Identify the preparation type.
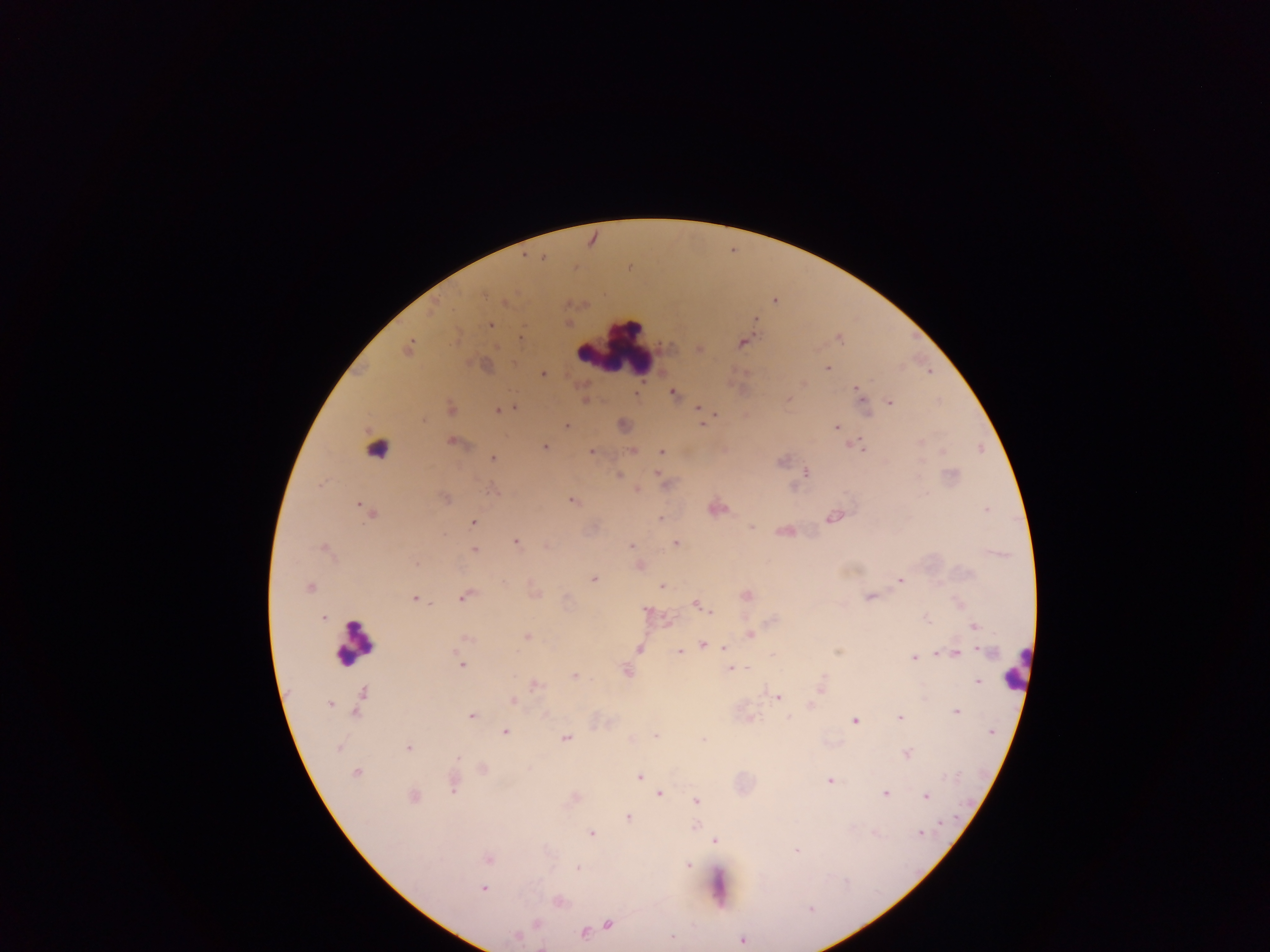
This is a thick smear.

Approximate centers as [x, y] in pixels.
Summary:
  - Malaria parasite locations: [543, 258], [774, 300], [503, 302], [755, 319], [490, 325], [519, 337], [741, 342], [408, 348], [699, 349], [827, 368], [542, 374], [857, 388], [672, 393], [638, 394], [862, 399], [584, 400], [787, 400], [889, 401], [450, 407], [515, 408], [698, 408], [496, 410], [717, 415], [703, 422], [565, 425], [836, 426], [452, 442], [854, 444], [544, 447], [632, 450], [590, 451], [662, 452], [492, 458], [655, 471], [806, 472], [618, 475], [636, 488], [444, 497], [572, 501], [987, 510], [368, 511], [833, 515], [661, 518], [472, 522], [785, 531], [515, 541], [676, 543], [545, 545], [631, 545], [326, 549], [473, 549], [637, 566], [594, 579], [899, 580], [661, 586], [309, 587], [745, 595], [465, 596], [870, 596], [414, 598], [696, 604], [646, 611], [710, 611], [321, 616], [925, 618], [974, 626], [750, 634], [526, 636], [466, 638], [702, 646], [724, 647], [639, 648], [679, 651], [955, 653], [914, 657], [460, 664], [729, 669], [626, 671], [574, 676], [978, 680], [535, 684], [821, 687], [776, 695], [360, 700], [513, 701], [329, 704], [810, 705], [956, 711], [543, 715], [471, 716], [900, 717], [748, 718], [854, 721], [505, 732], [656, 734], [566, 738], [702, 739], [408, 748], [907, 754], [482, 769], [356, 772], [640, 776], [830, 780], [452, 783], [658, 792], [884, 792], [413, 796], [925, 796], [573, 798], [695, 801], [629, 817], [694, 827], [591, 833], [919, 833], [714, 840], [797, 851], [488, 859], [687, 866], [576, 868], [483, 888], [557, 900], [536, 923], [608, 924], [595, 929], [582, 932], [517, 936], [741, 940]
  - Leukocyte locations: [617, 345], [376, 448], [354, 642], [1016, 672], [719, 885]
  - Image size: 1270×952 pixels
  - Field of view: single
  - Capture: mobile-phone photograph through a microscope
  - Country: Ghana